Locate every blood parasite and identify its species.
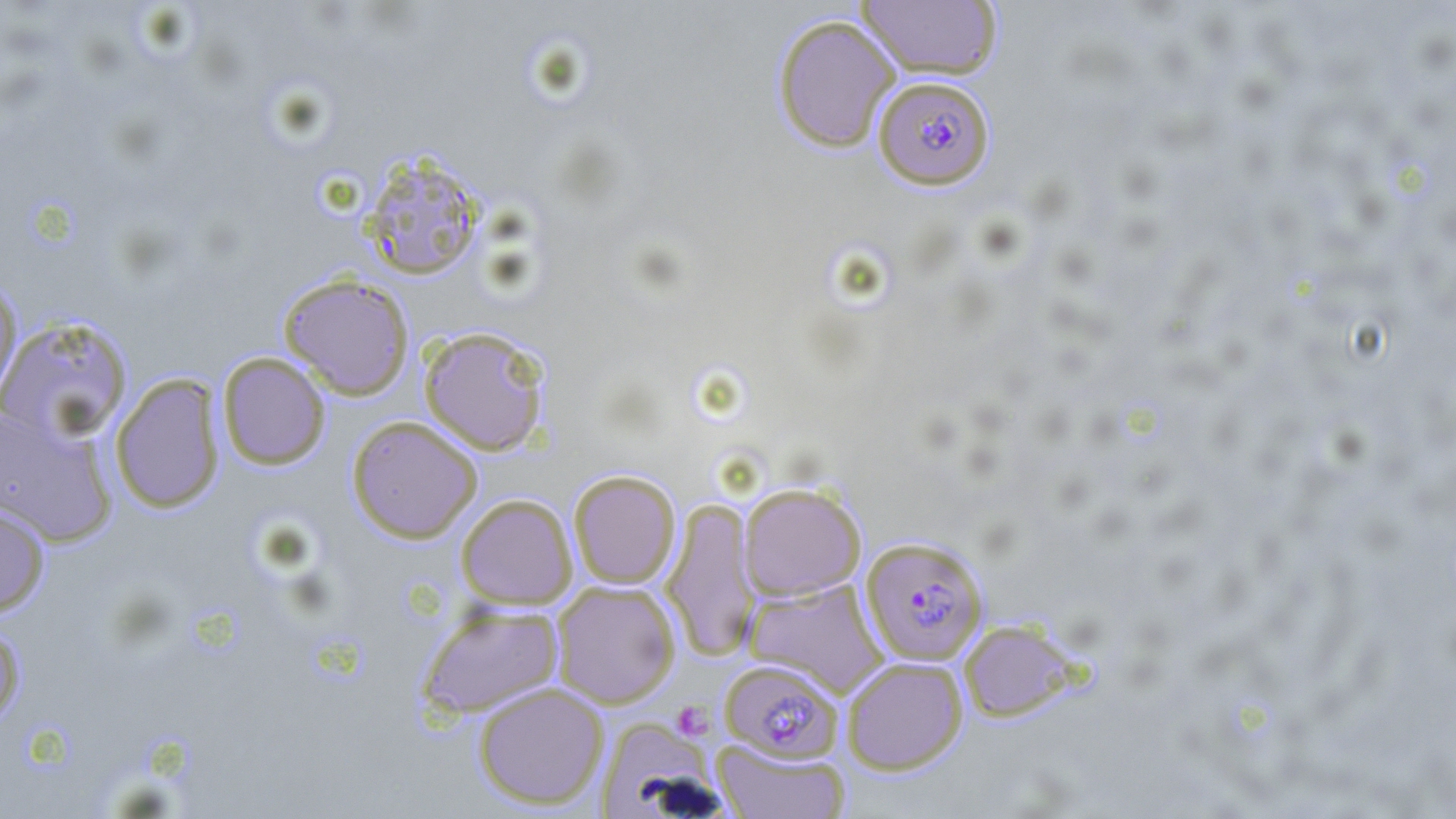
Approximate bounding boxes as named x1/y1/x2/y2 corners in pixels.
Plasmodium falciparum-infected red blood cells: (x1=872, y1=75, x2=995, y2=190), (x1=861, y1=536, x2=988, y2=665), (x1=718, y1=660, x2=842, y2=764).
No Plasmodium ovale, Plasmodium malariae, Plasmodium vivax, Babesia divergens, or Trypanosoma brucei observed.

Summary:
  - Platelet locations: (x1=671, y1=701, x2=715, y2=741)
  - Uninfected red blood cell locations: (x1=855, y1=1, x2=1003, y2=80), (x1=771, y1=14, x2=902, y2=153), (x1=360, y1=152, x2=486, y2=280), (x1=278, y1=272, x2=415, y2=400), (x1=0, y1=277, x2=22, y2=398), (x1=0, y1=315, x2=134, y2=444), (x1=418, y1=325, x2=552, y2=456), (x1=217, y1=352, x2=331, y2=470), (x1=110, y1=373, x2=225, y2=514), (x1=0, y1=406, x2=117, y2=547), (x1=346, y1=415, x2=483, y2=543), (x1=567, y1=469, x2=681, y2=589), (x1=738, y1=482, x2=866, y2=600), (x1=455, y1=493, x2=578, y2=610), (x1=661, y1=496, x2=760, y2=662), (x1=0, y1=503, x2=50, y2=617), (x1=744, y1=578, x2=888, y2=697), (x1=552, y1=580, x2=681, y2=709), (x1=416, y1=603, x2=564, y2=720), (x1=959, y1=619, x2=1080, y2=723), (x1=0, y1=623, x2=26, y2=725), (x1=841, y1=656, x2=968, y2=775), (x1=472, y1=681, x2=610, y2=810), (x1=593, y1=715, x2=722, y2=816), (x1=711, y1=739, x2=852, y2=819)
  - Slide-level diagnosis: Plasmodium falciparum
  - Field of view: one of a larger specimen
  - Modality: optical microscopy
  - Preparation: thin blood smear
  - Magnification: 1000x
  - Image size: 1456×819 pixels
  - Stain: May-Grünwald-Giemsa